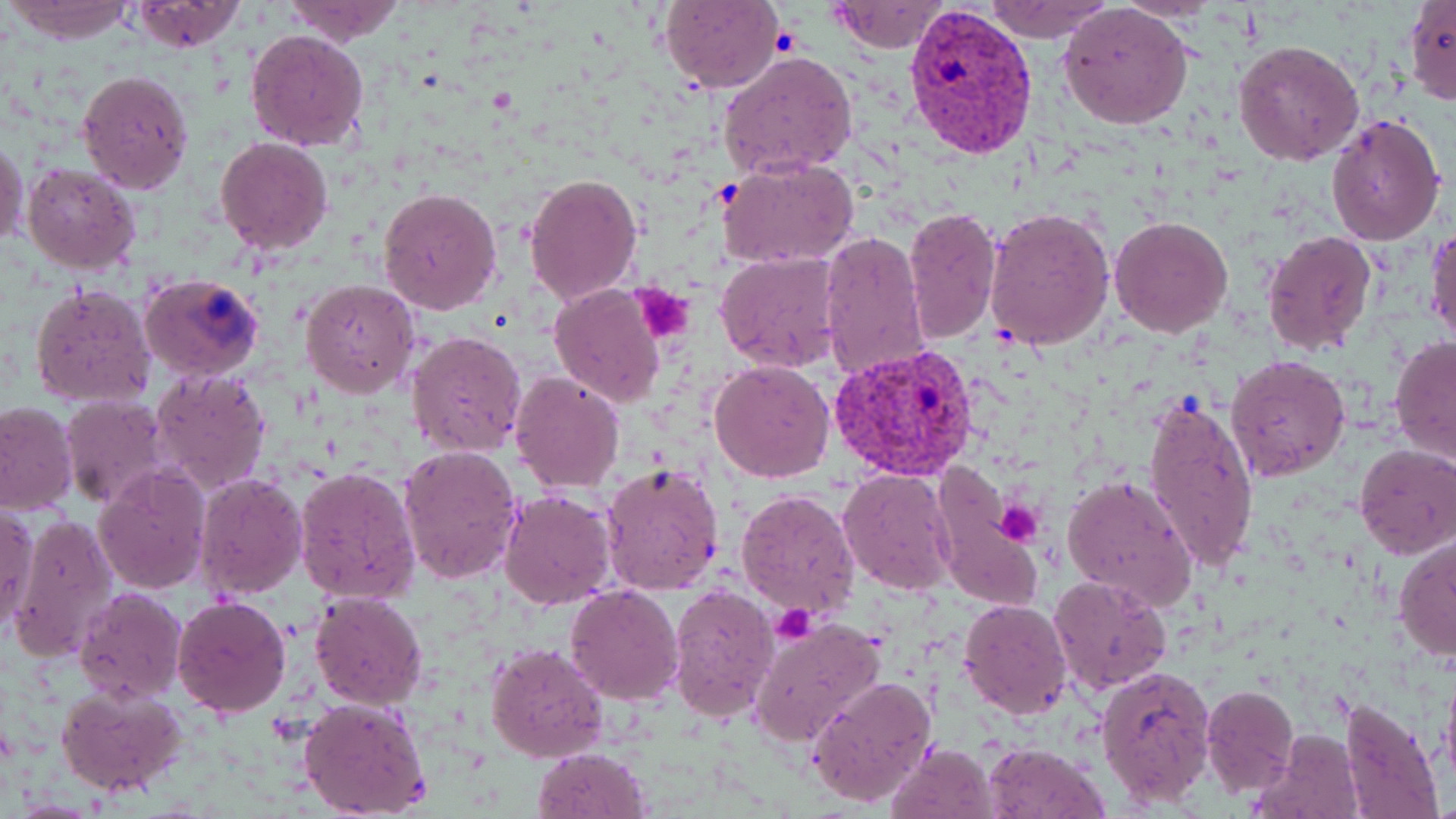
slide-level diagnosis = Plasmodium vivax
uninfected red blood cell locations = approximate bounding boxes as named x1/y1/x2/y2 corners in pixels: (x1=5, y1=0, x2=136, y2=44), (x1=278, y1=0, x2=408, y2=45), (x1=660, y1=0, x2=784, y2=93), (x1=124, y1=1, x2=250, y2=54), (x1=827, y1=1, x2=949, y2=54), (x1=982, y1=1, x2=1113, y2=42), (x1=1403, y1=1, x2=1456, y2=106), (x1=1059, y1=3, x2=1193, y2=131), (x1=245, y1=29, x2=370, y2=151), (x1=1233, y1=40, x2=1365, y2=165), (x1=719, y1=51, x2=858, y2=178), (x1=76, y1=69, x2=195, y2=194), (x1=1325, y1=112, x2=1446, y2=247), (x1=215, y1=137, x2=333, y2=253), (x1=0, y1=138, x2=29, y2=250), (x1=718, y1=156, x2=859, y2=270), (x1=22, y1=161, x2=141, y2=273), (x1=524, y1=171, x2=641, y2=306), (x1=379, y1=186, x2=504, y2=317), (x1=984, y1=205, x2=1114, y2=350), (x1=904, y1=208, x2=1003, y2=342), (x1=1108, y1=215, x2=1234, y2=338), (x1=1427, y1=221, x2=1455, y2=351), (x1=819, y1=231, x2=932, y2=383), (x1=1262, y1=231, x2=1377, y2=355), (x1=715, y1=251, x2=843, y2=374), (x1=300, y1=279, x2=420, y2=399), (x1=30, y1=282, x2=158, y2=410), (x1=549, y1=284, x2=665, y2=407), (x1=406, y1=331, x2=528, y2=459), (x1=1389, y1=336, x2=1456, y2=465), (x1=1226, y1=354, x2=1350, y2=482), (x1=709, y1=361, x2=836, y2=482), (x1=149, y1=368, x2=273, y2=496), (x1=510, y1=371, x2=625, y2=493), (x1=1144, y1=390, x2=1259, y2=579), (x1=58, y1=396, x2=171, y2=510), (x1=0, y1=400, x2=79, y2=513), (x1=1355, y1=444, x2=1456, y2=558), (x1=396, y1=445, x2=524, y2=584), (x1=599, y1=462, x2=725, y2=595), (x1=293, y1=465, x2=421, y2=607), (x1=93, y1=466, x2=212, y2=594), (x1=839, y1=469, x2=957, y2=593), (x1=193, y1=470, x2=308, y2=600), (x1=1063, y1=473, x2=1199, y2=614), (x1=937, y1=478, x2=1036, y2=605), (x1=734, y1=487, x2=860, y2=621), (x1=500, y1=491, x2=616, y2=609), (x1=1, y1=504, x2=40, y2=633), (x1=10, y1=514, x2=118, y2=662), (x1=1395, y1=537, x2=1456, y2=662), (x1=1047, y1=574, x2=1174, y2=696), (x1=565, y1=584, x2=684, y2=704), (x1=667, y1=584, x2=778, y2=721), (x1=75, y1=587, x2=187, y2=703), (x1=309, y1=591, x2=427, y2=710), (x1=173, y1=596, x2=291, y2=717), (x1=957, y1=598, x2=1072, y2=719), (x1=748, y1=617, x2=887, y2=746), (x1=485, y1=641, x2=608, y2=764), (x1=1094, y1=664, x2=1217, y2=807), (x1=1441, y1=670, x2=1456, y2=788), (x1=806, y1=675, x2=937, y2=810), (x1=56, y1=682, x2=187, y2=799), (x1=1201, y1=686, x2=1298, y2=797), (x1=299, y1=698, x2=431, y2=817), (x1=1338, y1=698, x2=1443, y2=819), (x1=1253, y1=728, x2=1364, y2=819), (x1=981, y1=742, x2=1107, y2=819), (x1=886, y1=743, x2=999, y2=819), (x1=533, y1=747, x2=652, y2=819)
field of view = single
modality = optical microscopy
magnification = 1000x
Plasmodium vivax-infected red blood cell locations = approximate bounding boxes as named x1/y1/x2/y2 corners in pixels: (x1=904, y1=4, x2=1039, y2=157), (x1=141, y1=272, x2=265, y2=381), (x1=829, y1=342, x2=979, y2=483)
image size = 1456×819 pixels
stain = May-Grünwald-Giemsa
preparation = thin blood smear
platelet locations = approximate bounding boxes as named x1/y1/x2/y2 corners in pixels: (x1=633, y1=285, x2=694, y2=344), (x1=994, y1=502, x2=1043, y2=545), (x1=771, y1=604, x2=816, y2=644)